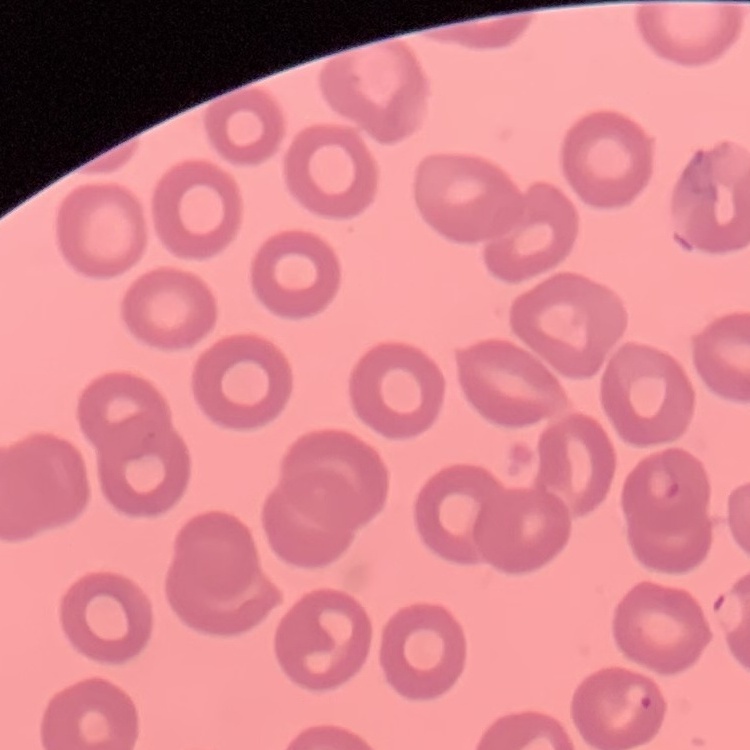
red blood cell morphology = no rouleaux formation
preparation = thin blood smear
image type = one tile cut from a larger photomicrograph
stain = Field's or Giemsa